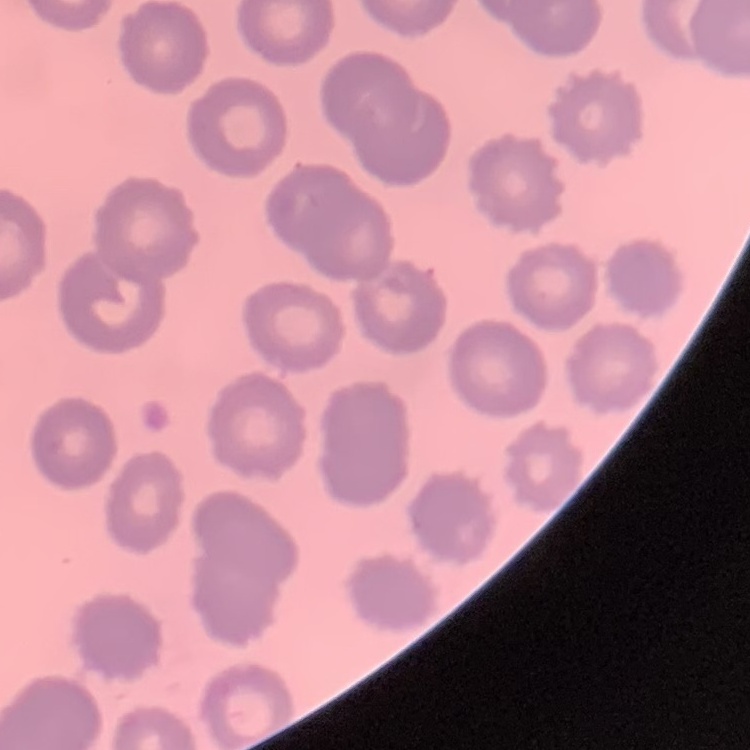
erythrocyte_morphology: no rouleaux formation
image_type: square crop of a larger photomicrograph
preparation: thin peripheral smear
stain: Field's or Giemsa